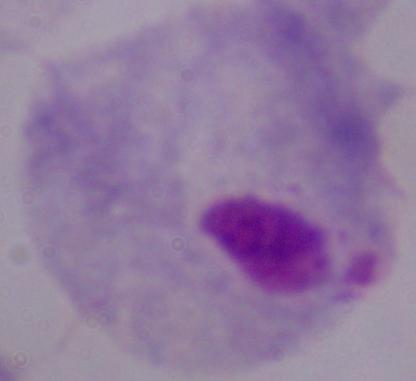
Summary:
  - Modality: micrograph
  - Magnification: 1000x
  - Identification: trichomonad